Assess this cell for malaria.
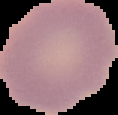

Uninfected.

Summary:
  - Image type: segmented cell region with the area outside set to black
  - Preparation: thin blood film
  - Image size: 118×115 pixels